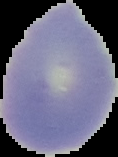

preparation: thin blood film
image_size: 118×157 pixels
result: no Plasmodium parasites seen
image_type: segmented cell region on a black background